Assess for Plasmodium parasites.
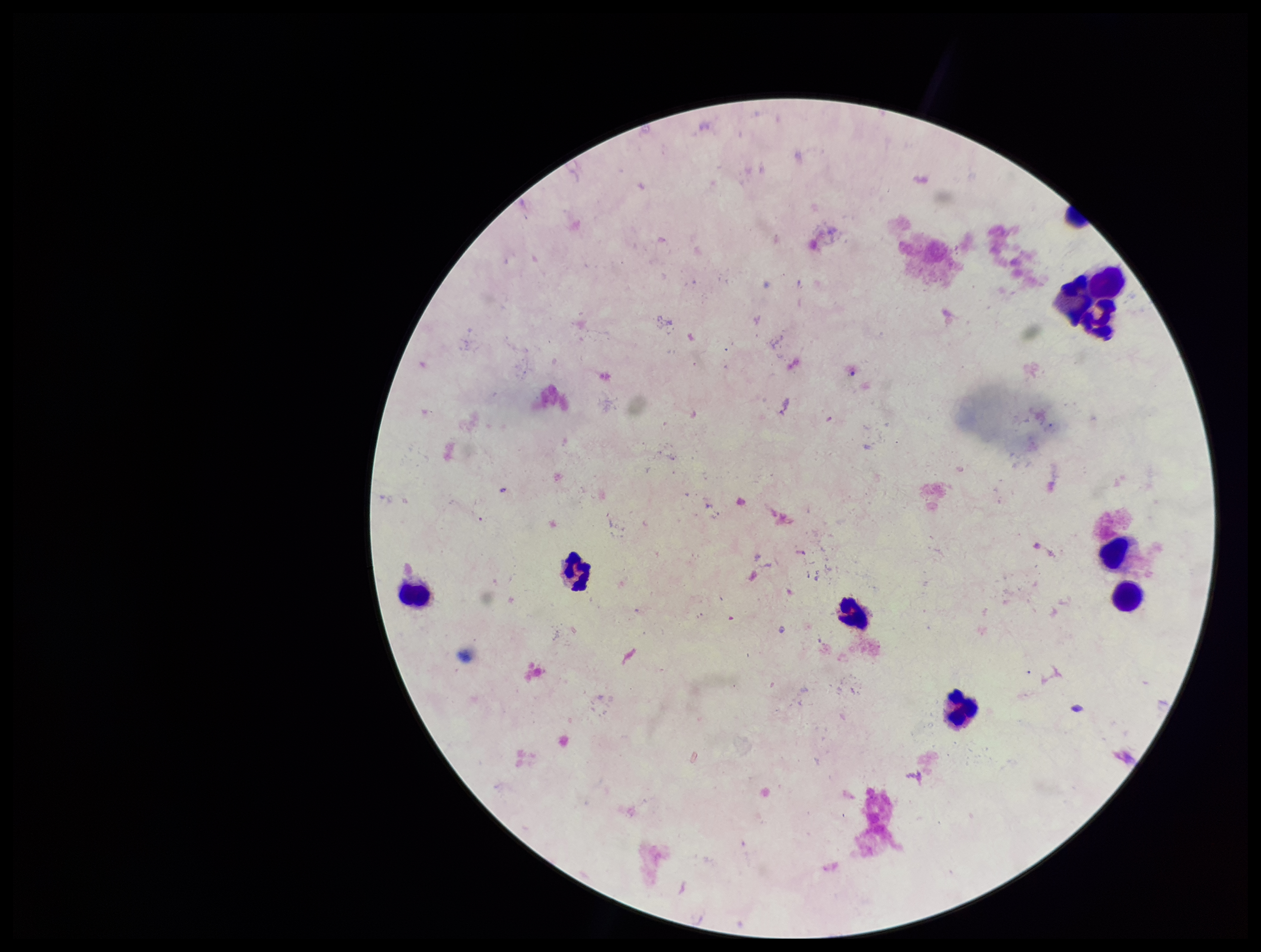
None identified.

stain: Giemsa
capture: smartphone photograph through the microscope eyepiece
image_size: 1261×952 pixels
leukocyte_count: 7
parasite_count: 0
patient_malaria_status: negative
preparation: thick smear
field_of_view: one from this slide